Describe the morphology of the erythrocytes.
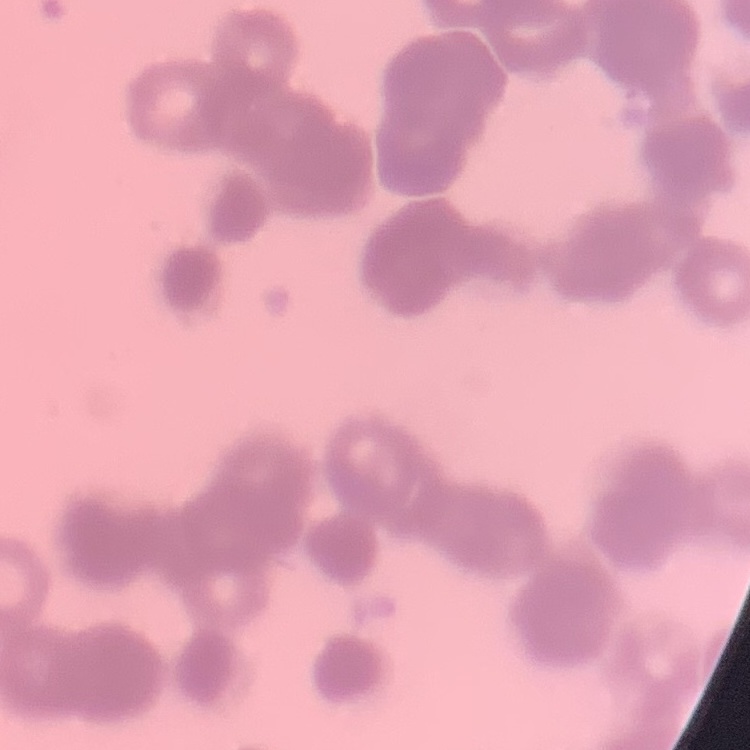
Rouleaux formation.

stain = Field's or Giemsa
image type = square crop of a larger photomicrograph
preparation = thin blood film